Describe the morphology of the erythrocytes.
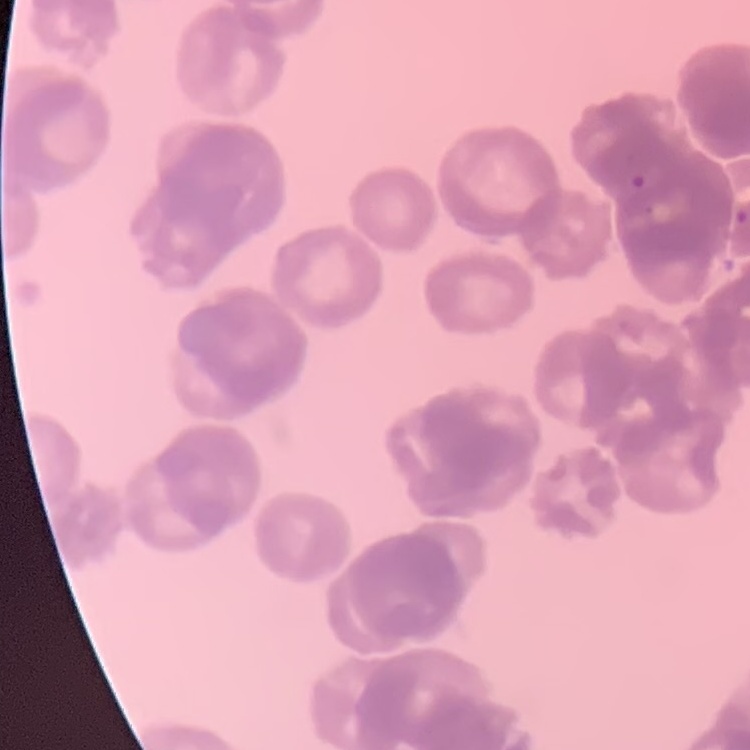

Rouleaux formation.

Thin blood smear. One tile cut from a larger photomicrograph. Stained with either Field's or Giemsa.